Describe the morphology of the red blood cells.
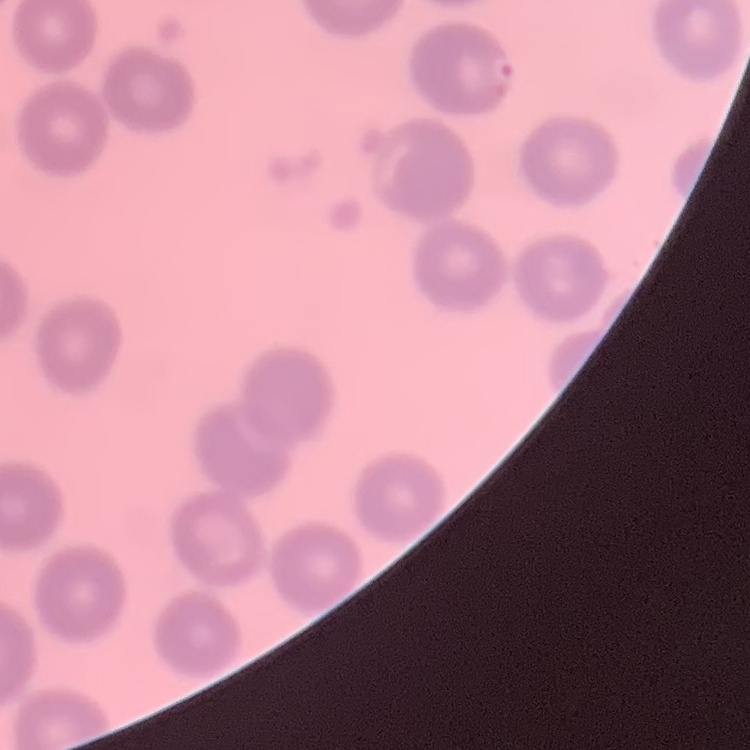

They show no rouleaux formation.

image type = one tile cut from a larger photomicrograph
stain = Field's or Giemsa
preparation = thin peripheral smear